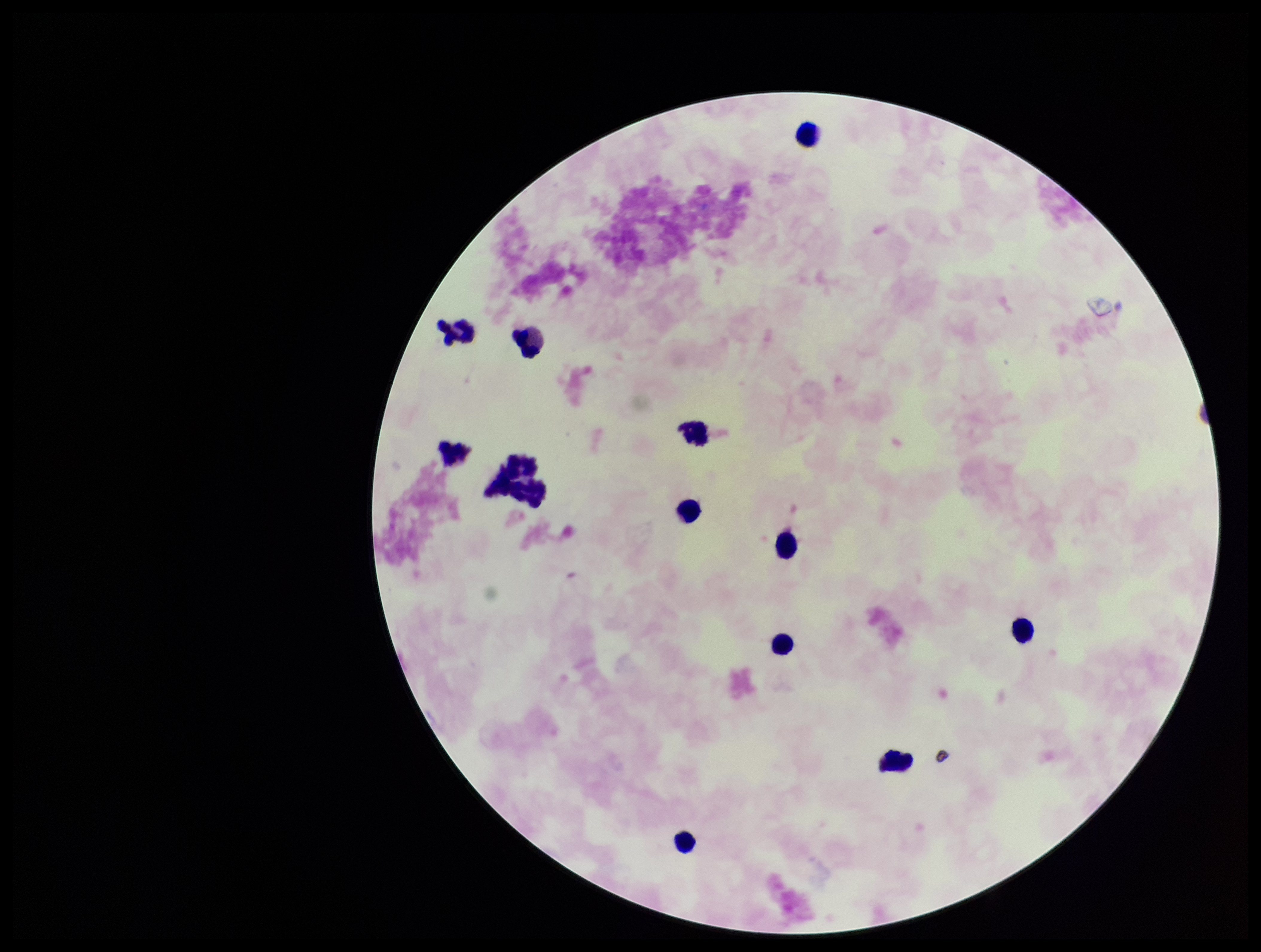

{
  "leukocyte_count": 12,
  "field_of_view": "single",
  "patient_malaria_status": "negative",
  "image_size": "1261×952 pixels",
  "parasite_count": 0,
  "stain": "Giemsa",
  "preparation": "thick",
  "plasmodium_parasites": "none identified",
  "capture": "smartphone photograph through the microscope eyepiece"
}